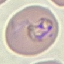 Malaria status: parasitized. Acquired by smartphone through the microscope eyepiece. Thin blood film. Automatically extracted cell patch, resized to 64 × 64 pixels. Giemsa stain.